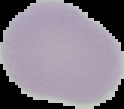

Summary:
  - Image size: 124×109 pixels
  - Result: negative for malaria parasites
  - Image type: segmented cell region with the area outside set to black
  - Preparation: thin blood film